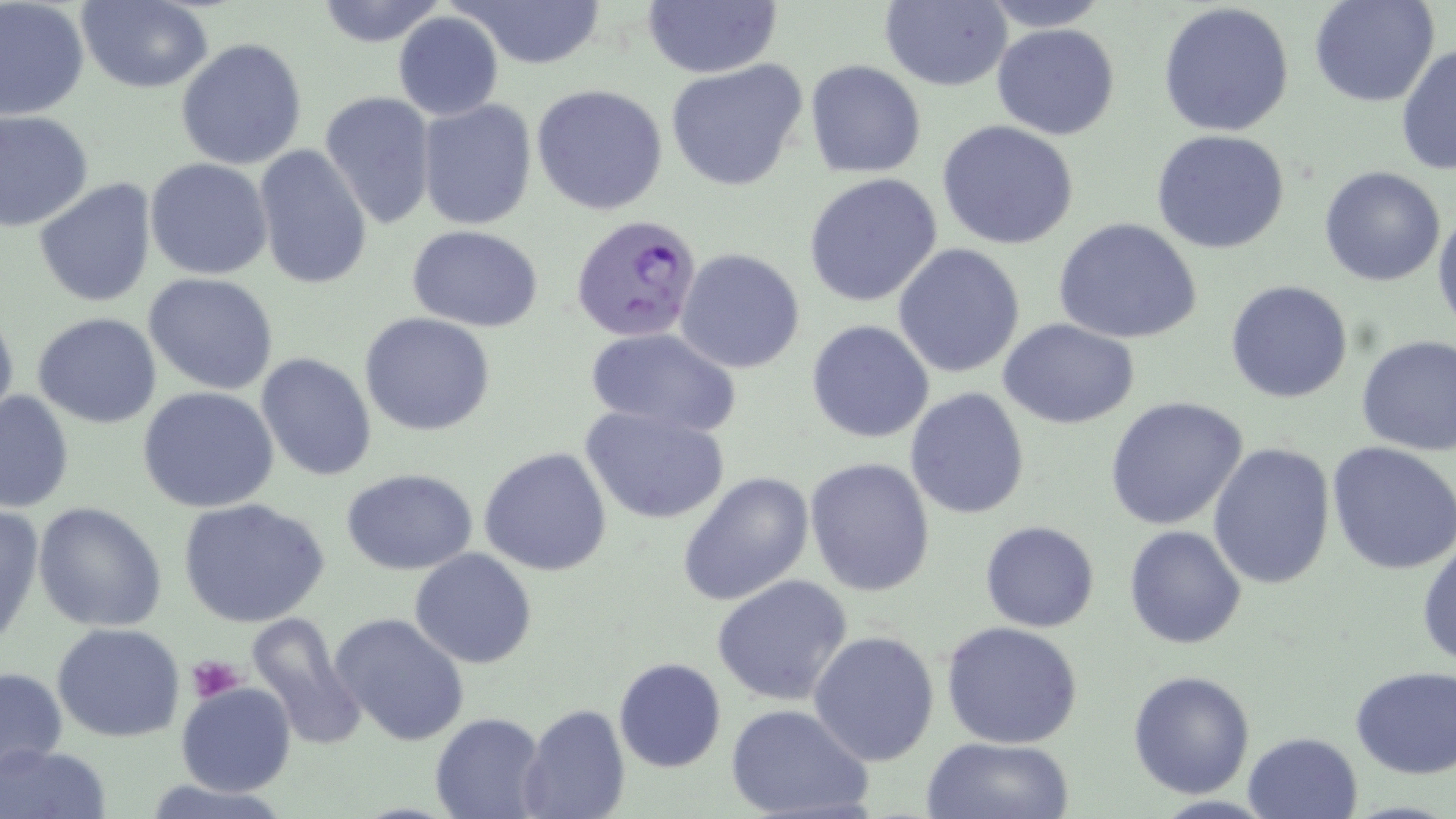

Approximate bounding boxes as named x1/y1/x2/y2 corners in pixels. Plasmodium falciparum-infected red blood cell locations: (x1=572, y1=212, x2=704, y2=341). Platelet locations: (x1=188, y1=651, x2=246, y2=702). Uninfected red blood cell locations: (x1=0, y1=0, x2=90, y2=120), (x1=76, y1=0, x2=213, y2=94), (x1=313, y1=0, x2=450, y2=47), (x1=453, y1=0, x2=608, y2=70), (x1=879, y1=0, x2=1011, y2=90), (x1=982, y1=0, x2=1113, y2=33), (x1=1306, y1=0, x2=1441, y2=109), (x1=642, y1=2, x2=783, y2=79), (x1=1156, y1=3, x2=1297, y2=137), (x1=392, y1=11, x2=504, y2=121), (x1=991, y1=21, x2=1121, y2=141), (x1=175, y1=38, x2=308, y2=171), (x1=1396, y1=45, x2=1455, y2=176), (x1=665, y1=60, x2=809, y2=191), (x1=805, y1=60, x2=927, y2=180), (x1=531, y1=83, x2=670, y2=216), (x1=319, y1=90, x2=436, y2=228), (x1=417, y1=100, x2=537, y2=231), (x1=0, y1=108, x2=95, y2=232), (x1=937, y1=119, x2=1081, y2=250), (x1=1150, y1=129, x2=1290, y2=254), (x1=254, y1=145, x2=373, y2=293), (x1=145, y1=157, x2=273, y2=280), (x1=1318, y1=164, x2=1449, y2=286), (x1=803, y1=172, x2=945, y2=308), (x1=33, y1=178, x2=157, y2=307), (x1=1432, y1=205, x2=1456, y2=335), (x1=1053, y1=217, x2=1204, y2=344), (x1=405, y1=223, x2=546, y2=331), (x1=892, y1=242, x2=1026, y2=378), (x1=675, y1=247, x2=806, y2=374), (x1=143, y1=272, x2=278, y2=394), (x1=1225, y1=279, x2=1355, y2=404), (x1=0, y1=303, x2=18, y2=431), (x1=32, y1=312, x2=162, y2=428), (x1=359, y1=313, x2=497, y2=437), (x1=998, y1=317, x2=1140, y2=429), (x1=805, y1=320, x2=936, y2=444), (x1=586, y1=327, x2=740, y2=438), (x1=1355, y1=334, x2=1456, y2=455), (x1=255, y1=353, x2=377, y2=481), (x1=136, y1=386, x2=281, y2=515), (x1=905, y1=387, x2=1033, y2=521), (x1=0, y1=390, x2=74, y2=514), (x1=1104, y1=395, x2=1249, y2=530), (x1=580, y1=403, x2=731, y2=525), (x1=1207, y1=441, x2=1337, y2=590), (x1=1328, y1=441, x2=1456, y2=576), (x1=479, y1=446, x2=612, y2=577), (x1=803, y1=456, x2=935, y2=597), (x1=340, y1=469, x2=481, y2=575), (x1=677, y1=471, x2=814, y2=607), (x1=178, y1=496, x2=334, y2=631), (x1=31, y1=501, x2=168, y2=632), (x1=0, y1=504, x2=45, y2=650), (x1=980, y1=521, x2=1102, y2=633), (x1=1124, y1=524, x2=1250, y2=650), (x1=1416, y1=530, x2=1456, y2=670), (x1=409, y1=548, x2=538, y2=669), (x1=711, y1=574, x2=854, y2=706), (x1=247, y1=613, x2=369, y2=748), (x1=329, y1=613, x2=470, y2=747), (x1=941, y1=622, x2=1083, y2=750), (x1=52, y1=623, x2=186, y2=741), (x1=809, y1=629, x2=942, y2=766), (x1=613, y1=658, x2=727, y2=772), (x1=1349, y1=665, x2=1456, y2=778), (x1=0, y1=666, x2=68, y2=773), (x1=1128, y1=669, x2=1255, y2=797), (x1=178, y1=682, x2=295, y2=796), (x1=516, y1=703, x2=630, y2=819), (x1=726, y1=704, x2=875, y2=818), (x1=429, y1=713, x2=545, y2=819), (x1=1243, y1=731, x2=1364, y2=819), (x1=922, y1=735, x2=1075, y2=819), (x1=0, y1=743, x2=109, y2=819), (x1=139, y1=778, x2=295, y2=817). Slide-level diagnosis: Plasmodium falciparum. Thin blood smear. Image is 1456×819 pixels. One field of a larger specimen. Light microscopy. May-Grünwald-Giemsa-stained preparation. Captured at 1000x magnification.